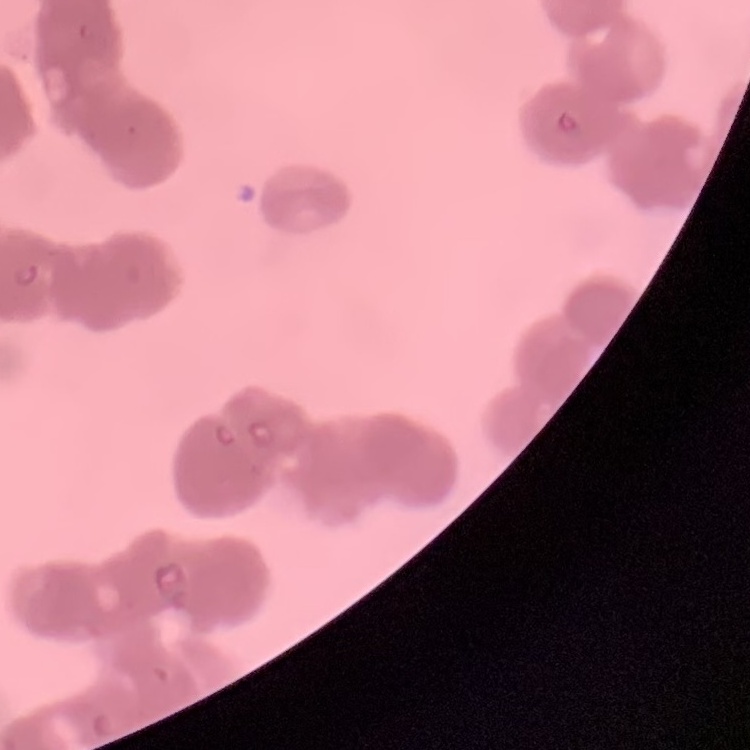

red blood cell morphology = rouleaux formation
preparation = thin blood smear
stain = Field's or Giemsa
image type = one tile cut from a larger photomicrograph